Assess this cell for malaria.
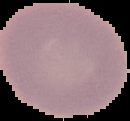

Uninfected.

{
  "preparation": "thin blood film",
  "image_size": "130×121 pixels",
  "image_type": "segmented cell region with the area outside set to black"
}